Point out every malaria parasite.
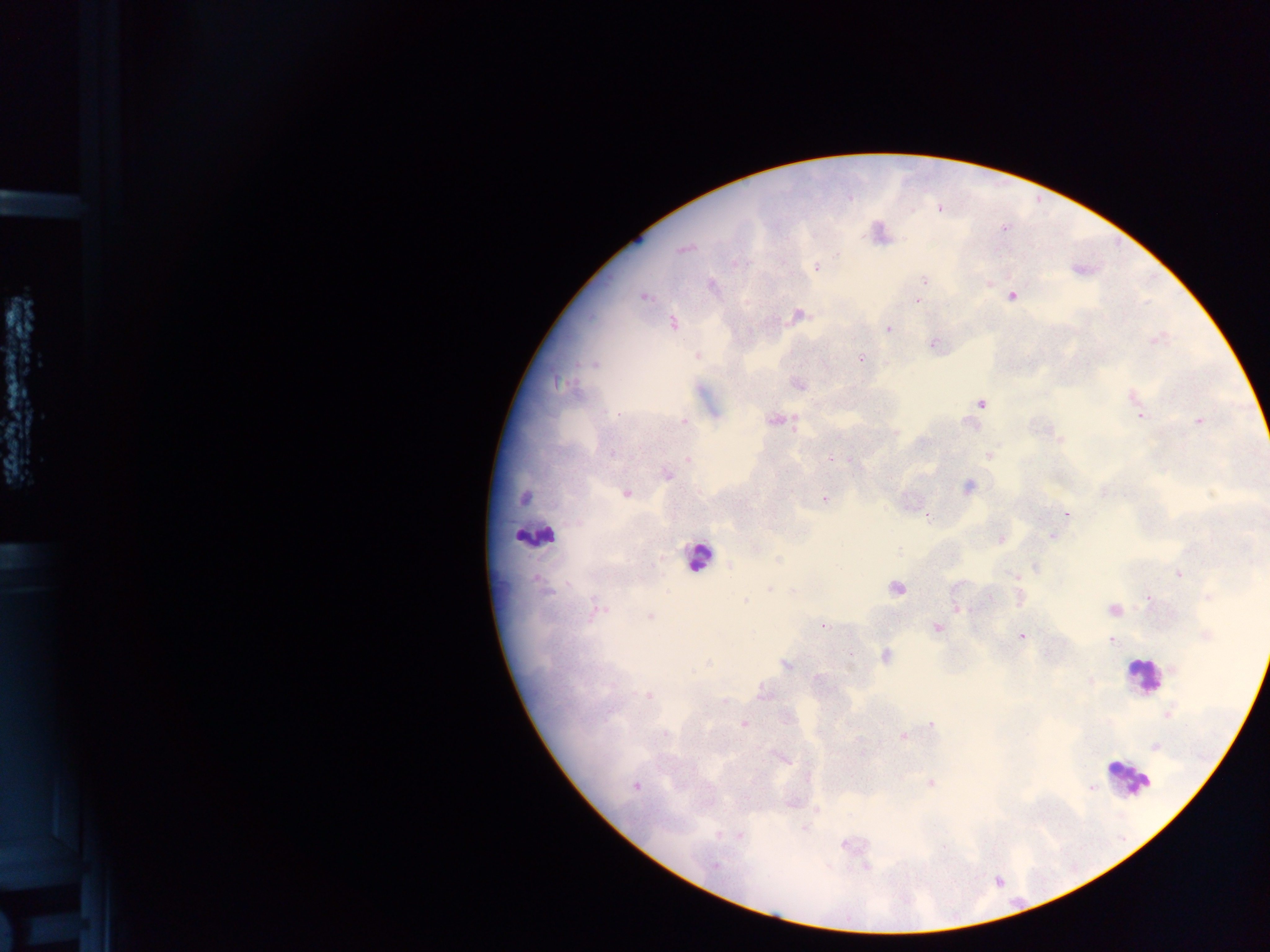
Approximate centers as (x, y) in pixels.
Malaria parasites: (939, 209), (1003, 228), (684, 249), (737, 263), (817, 268), (924, 279), (989, 284), (712, 285), (920, 290), (643, 296), (1012, 296), (917, 300), (798, 315), (673, 324), (888, 329), (1156, 340), (932, 345), (697, 356), (861, 358), (593, 364), (560, 384), (798, 385), (1132, 397), (981, 404), (617, 414), (1140, 416), (774, 420), (1199, 421), (684, 422), (895, 431), (1059, 437), (612, 453), (990, 454), (831, 459), (689, 460), (666, 475), (968, 487), (626, 493), (1104, 493), (524, 498), (825, 499), (1066, 514), (927, 515), (1051, 536), (1001, 539), (755, 548), (898, 550), (778, 559), (730, 566), (1036, 568), (1179, 574), (1014, 575), (770, 588), (896, 588), (1209, 596), (1020, 598), (1149, 598), (989, 599), (745, 600), (600, 609), (957, 609), (1113, 610), (650, 617), (823, 625), (937, 628), (1022, 636), (1205, 636), (1112, 641), (885, 656), (708, 664), (786, 666), (1174, 669), (818, 678), (1091, 681), (763, 693), (648, 696), (725, 701), (1168, 714), (785, 718), (743, 723), (932, 725), (665, 734), (903, 736), (1155, 747), (782, 759), (931, 784), (636, 785), (1090, 787), (816, 809), (718, 835), (739, 835), (845, 845), (716, 865).

preparation: thick blood smear
country: Ghana
field_of_view: single
leukocyte_locations: 'approximate centers as (x, y) in pixels: (531, 532), (698, 557), (1142, 676), (1129, 778)'
image_size: 1270×952 pixels
capture: mobile-phone photograph through a microscope